Classify the preparation.
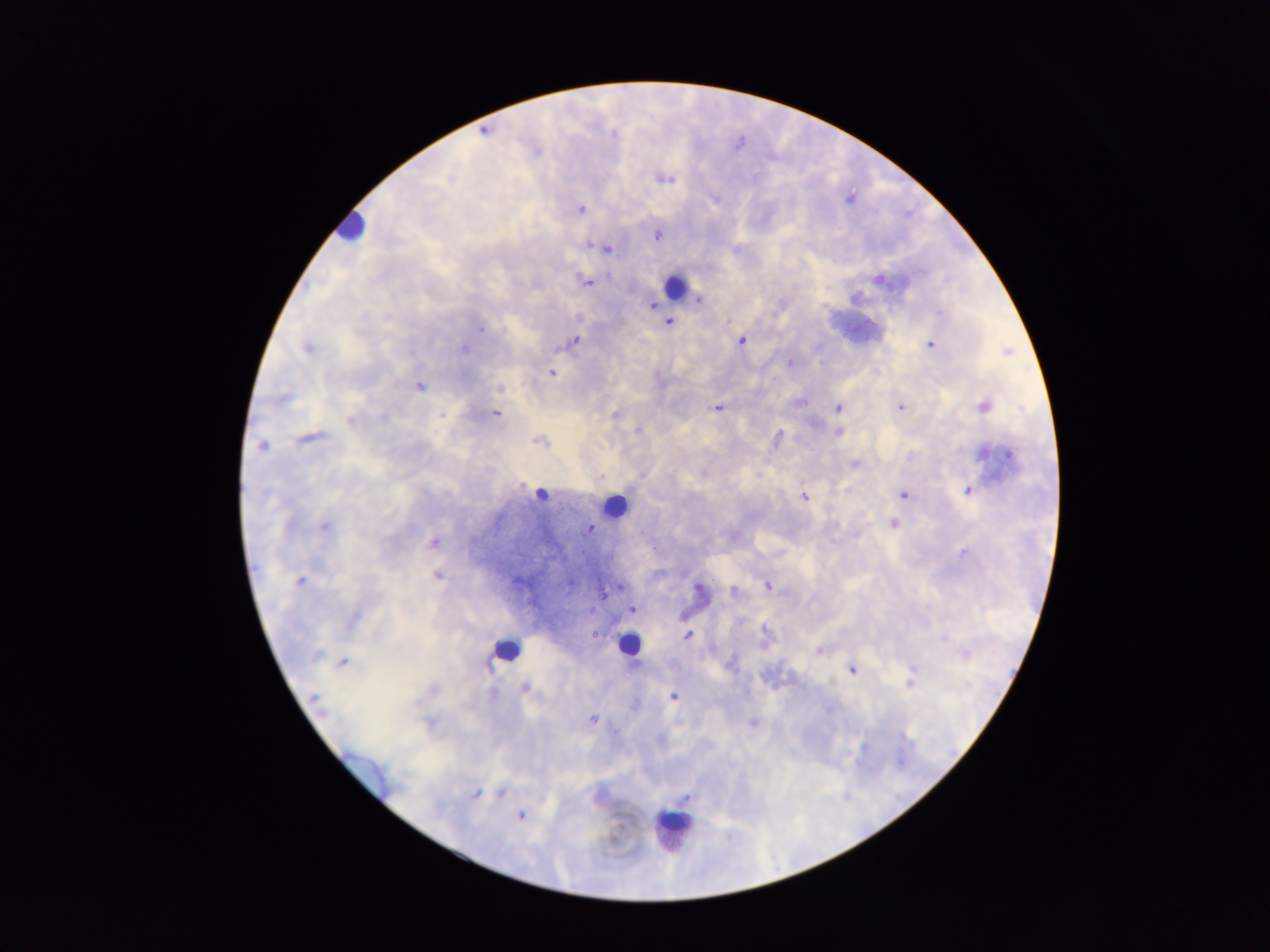

This is a thick smear.

Approximate centers as x y in pixels. Malaria parasite locations: 614 134; 664 178; 580 208; 657 235; 591 244; 607 247; 878 280; 585 281; 698 299; 653 305; 669 323; 481 329; 574 341; 741 341; 931 345; 306 349; 464 349; 791 363; 551 373; 419 387; 499 388; 282 399; 799 402; 983 406; 901 407; 838 408; 717 409; 496 413; 615 414; 442 416; 349 420; 638 430; 839 432; 310 438; 777 438; 538 441; 262 445; 910 456; 1001 456; 855 464; 601 477; 968 490; 903 495; 804 497; 892 524; 324 526; 590 529; 433 543; 963 554; 437 576; 300 580; 570 584; 767 587; 700 590; 734 591; 633 609; 353 618; 687 636; 820 651; 318 655; 343 662; 730 665; 853 670; 911 684; 525 687; 493 693; 672 697; 316 699; 593 720; 753 723; 502 794; 474 796; 686 798; 520 816. Leukocyte locations: 349 226; 674 285; 542 491; 614 505; 629 645; 505 650; 675 825. Collected in Ghana. Photographed through a microscope with a mobile-phone camera. Single field of view. Image is 1270×952 pixels.